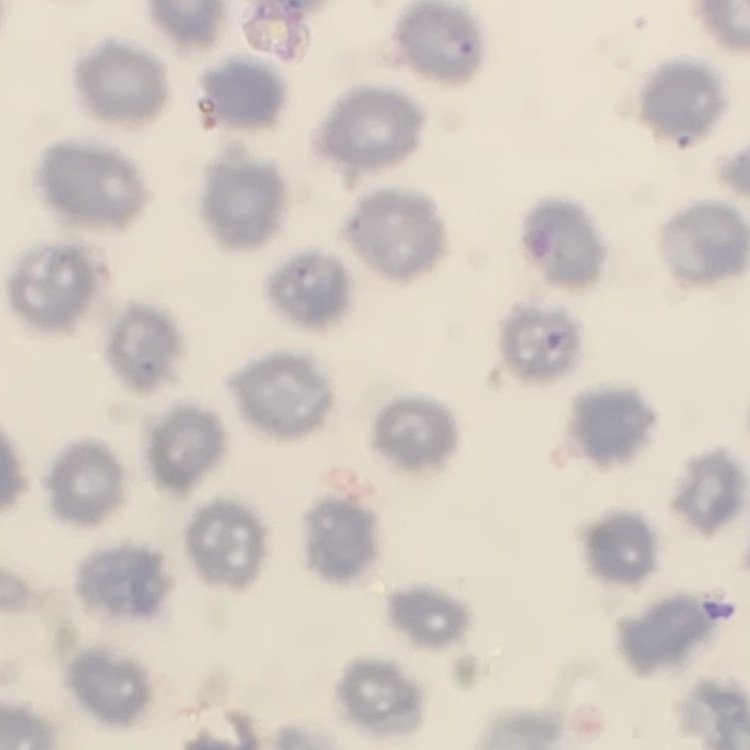
The red blood cells show no rouleaux formation. Thin blood smear. Stained with either Field's or Giemsa. Square crop of a larger photomicrograph.